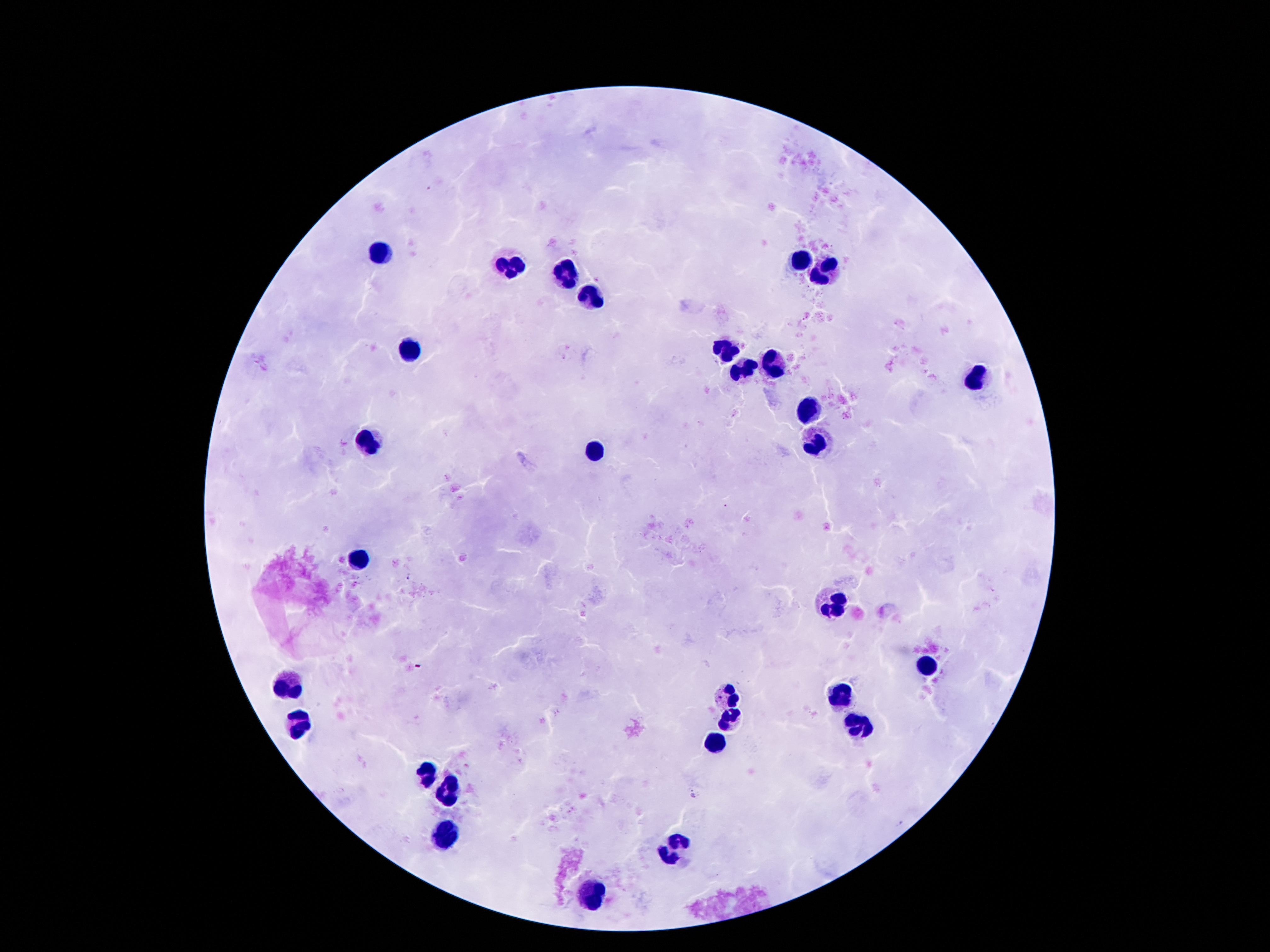

Approximate centers as (x, y) in pixels.
Summary:
  - Leukocyte locations: (379, 249), (801, 259), (510, 268), (825, 271), (567, 272), (594, 296), (410, 347), (721, 348), (774, 365), (737, 370), (975, 378), (807, 407), (369, 441), (817, 441), (596, 452), (360, 560), (835, 601), (925, 662), (289, 686), (727, 695), (840, 699), (731, 720), (299, 723), (862, 729), (713, 744), (426, 772), (446, 793), (446, 835), (676, 850), (594, 893)
  - Capture: smartphone camera through the microscope eyepiece
  - Magnification: 100x
  - Field of view: single
  - Patient malaria status: uninfected
  - Image size: 1270×952 pixels
  - Preparation: thick peripheral-blood smear
  - Stain: Giemsa